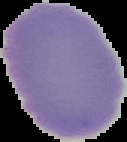
Result: no malaria parasites detected. From a thin blood film. The area outside the segmented cell region is set to black. Image is 127×142 pixels.